Locate every Plasmodium ovale-infected red blood cell.
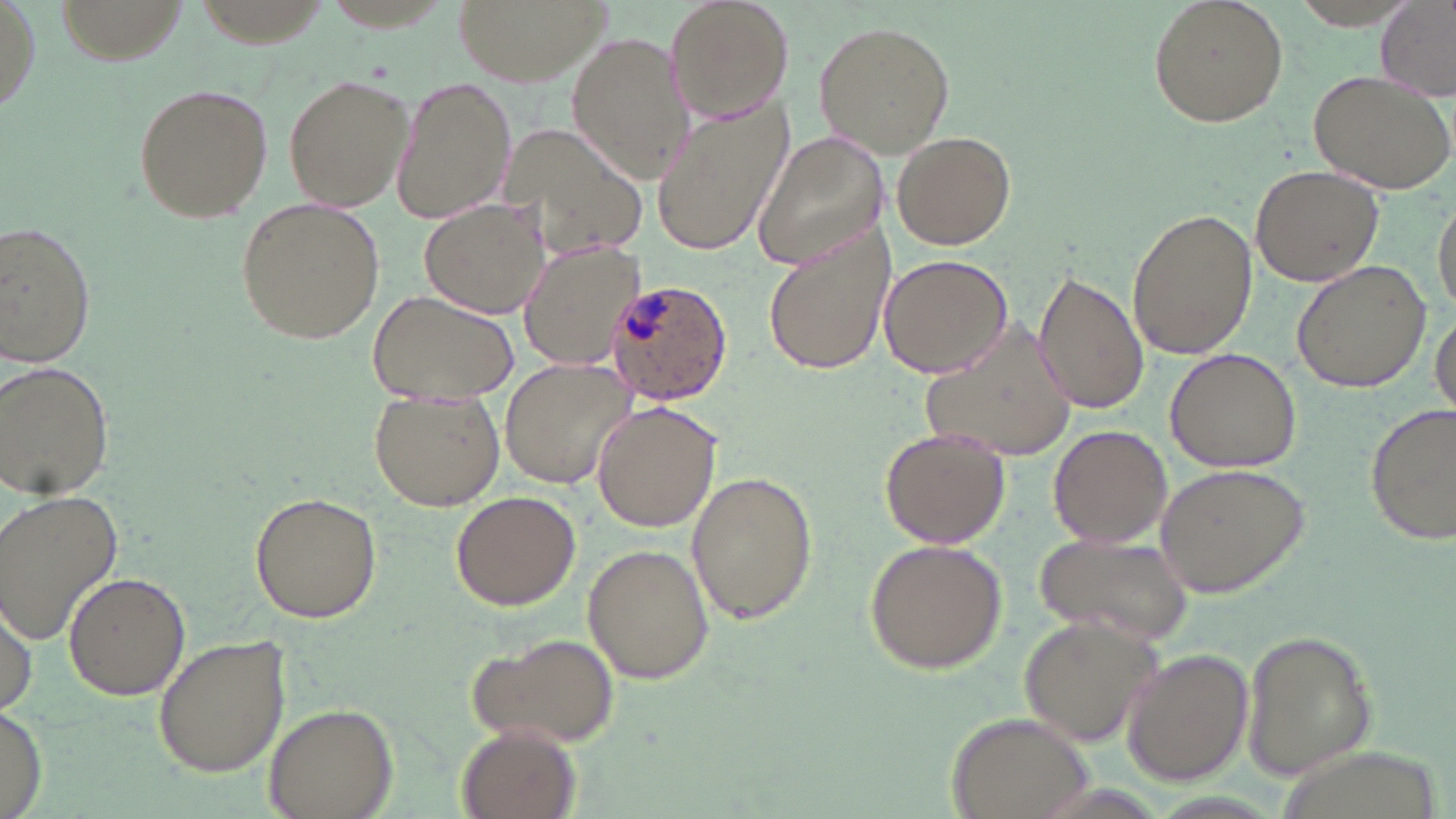

Approximate bounding boxes as (x1, y1, x2, y2) in pixels.
Plasmodium ovale-infected red blood cells: (607, 277, 735, 405).

Uninfected red blood cell locations: (452, 0, 611, 85), (664, 0, 796, 125), (1147, 0, 1288, 126), (54, 1, 188, 63), (1375, 1, 1455, 102), (811, 18, 956, 157), (567, 31, 697, 180), (1307, 69, 1456, 194), (282, 74, 412, 213), (391, 77, 516, 225), (133, 83, 271, 223), (649, 104, 791, 258), (495, 125, 647, 258), (754, 131, 891, 272), (889, 131, 1018, 250), (1251, 164, 1388, 287), (1432, 193, 1455, 319), (234, 195, 386, 344), (419, 199, 551, 319), (1127, 206, 1257, 361), (1, 219, 98, 367), (762, 226, 895, 378), (517, 240, 645, 370), (876, 253, 1013, 379), (1294, 259, 1431, 393), (1033, 270, 1147, 414), (366, 288, 519, 404), (1430, 308, 1455, 423), (915, 327, 1081, 460), (1164, 348, 1301, 472), (499, 358, 638, 490), (0, 359, 115, 502), (369, 392, 507, 511), (592, 401, 722, 534), (1365, 401, 1454, 544), (1047, 424, 1172, 548), (879, 429, 1011, 548), (1153, 462, 1313, 598), (686, 467, 820, 626), (0, 488, 125, 646), (448, 490, 582, 611), (249, 491, 382, 624), (1032, 534, 1191, 642), (864, 537, 1008, 674), (582, 544, 714, 684), (62, 573, 190, 700), (0, 594, 36, 716), (1017, 614, 1164, 750), (1241, 625, 1376, 782), (468, 630, 621, 750), (151, 632, 292, 777), (1122, 648, 1254, 784), (263, 701, 397, 819), (0, 705, 46, 817), (945, 709, 1098, 819), (456, 724, 580, 819). Slide-level diagnosis: Plasmodium ovale. One field of a larger specimen. Image is 1456×819 pixels. May-Grünwald-Giemsa-stained preparation. Thin blood film. 1000x magnification. Light microscopy.